Point out each malaria parasite.
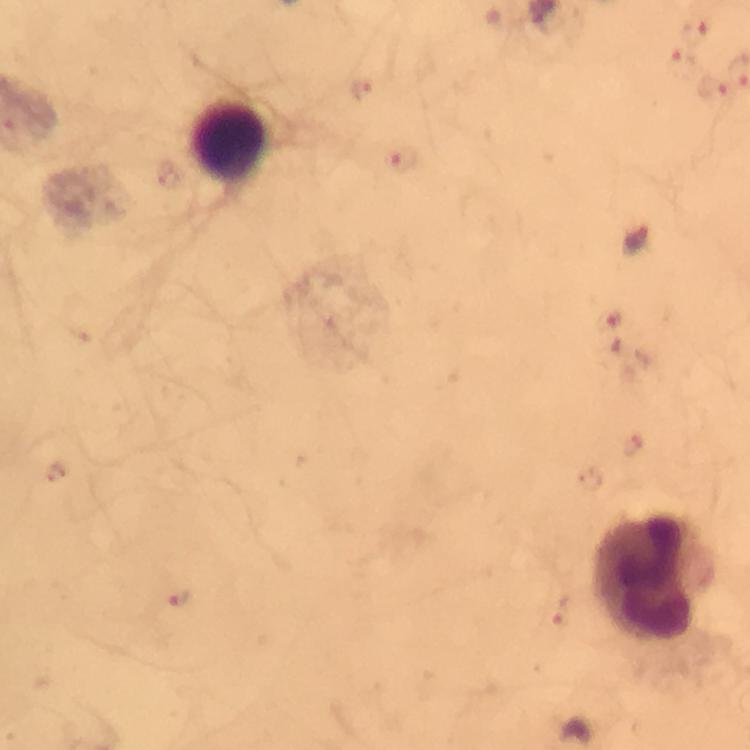

Approximate object centers, in pixels from the top-left corner.
Malaria parasites: (x=697, y=31), (x=679, y=65), (x=710, y=86), (x=637, y=241).

Leukocyte locations: (x=229, y=143), (x=651, y=578). Thick blood film. Giemsa-stained preparation. Image is 750×750 pixels. Immersion oil was used. From a malaria diagnostic workup. A crop from one field of view. Smartphone photograph taken through a microscope. At 100x magnification.